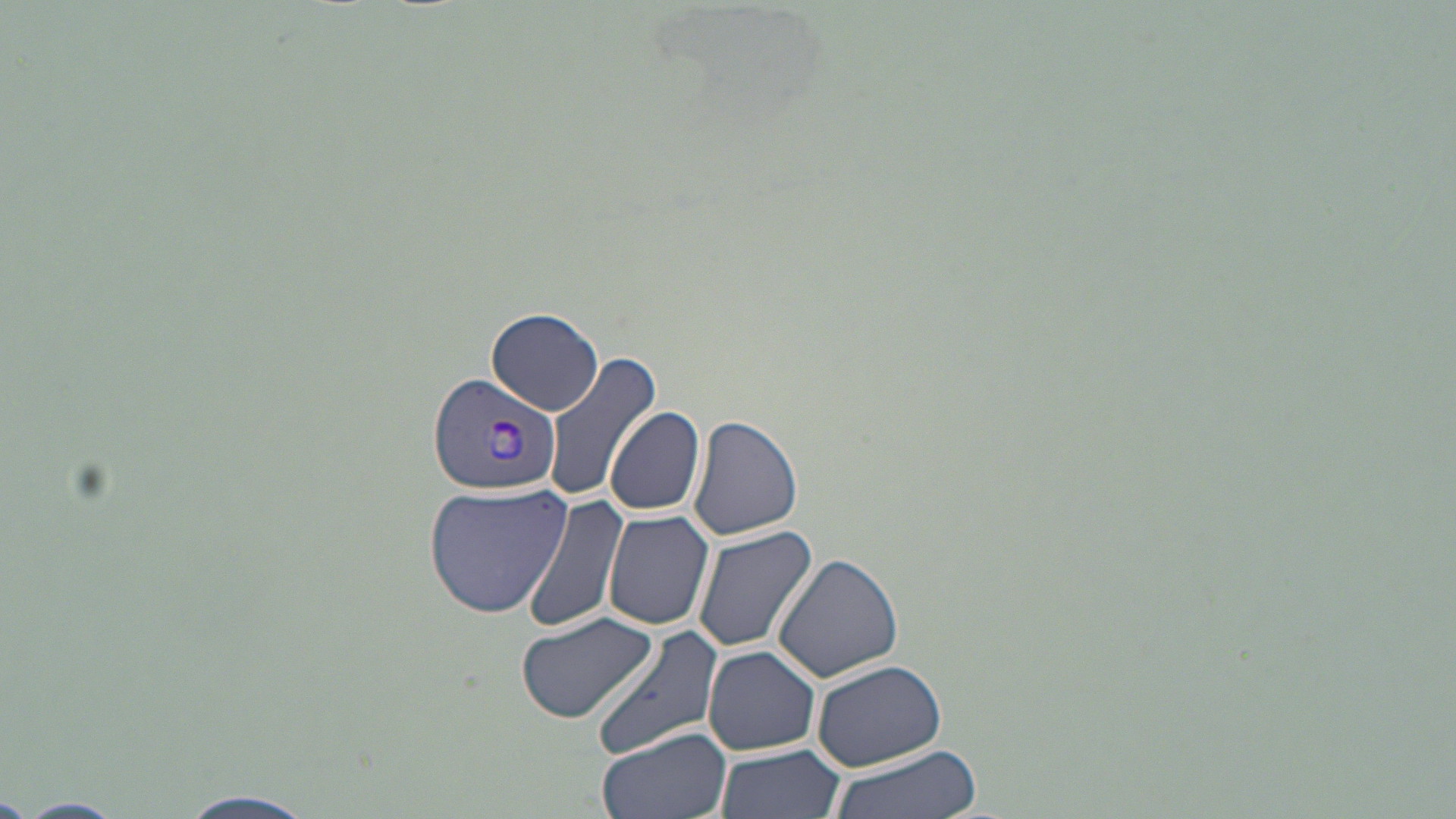 Approximate bounding boxes as (x1, y1, x2, y2) in pixels. Plasmodium vivax-infected red blood cell locations: (428, 371, 562, 496). Uninfected red blood cell locations: (486, 307, 604, 416), (544, 349, 661, 504), (607, 404, 706, 517), (688, 414, 805, 539), (422, 480, 574, 620), (521, 495, 627, 638), (603, 509, 716, 631), (692, 524, 820, 653), (773, 552, 906, 683), (516, 611, 662, 727), (590, 624, 724, 761), (702, 644, 821, 755), (809, 657, 948, 771), (595, 725, 733, 819), (714, 745, 846, 819), (823, 746, 983, 819), (176, 790, 324, 819), (12, 797, 125, 818). Slide-level diagnosis: Plasmodium vivax. May-Grünwald-Giemsa stain. Image is 1456×819 pixels. Thin blood smear. One field of a larger specimen. Optical microscopy. 1000x magnification.